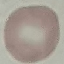

Result: no malaria parasites seen. Thin smear of blood. Automatically extracted cell patch, resized to 64 × 64 pixels. Giemsa-stained preparation. Acquired by smartphone through the microscope eyepiece.